Classify this cell by malaria status.
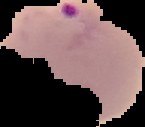
Parasitized.

Summary:
  - Preparation: thin blood smear
  - Image size: 145×127 pixels
  - Image type: segmented cell region with the area outside set to black